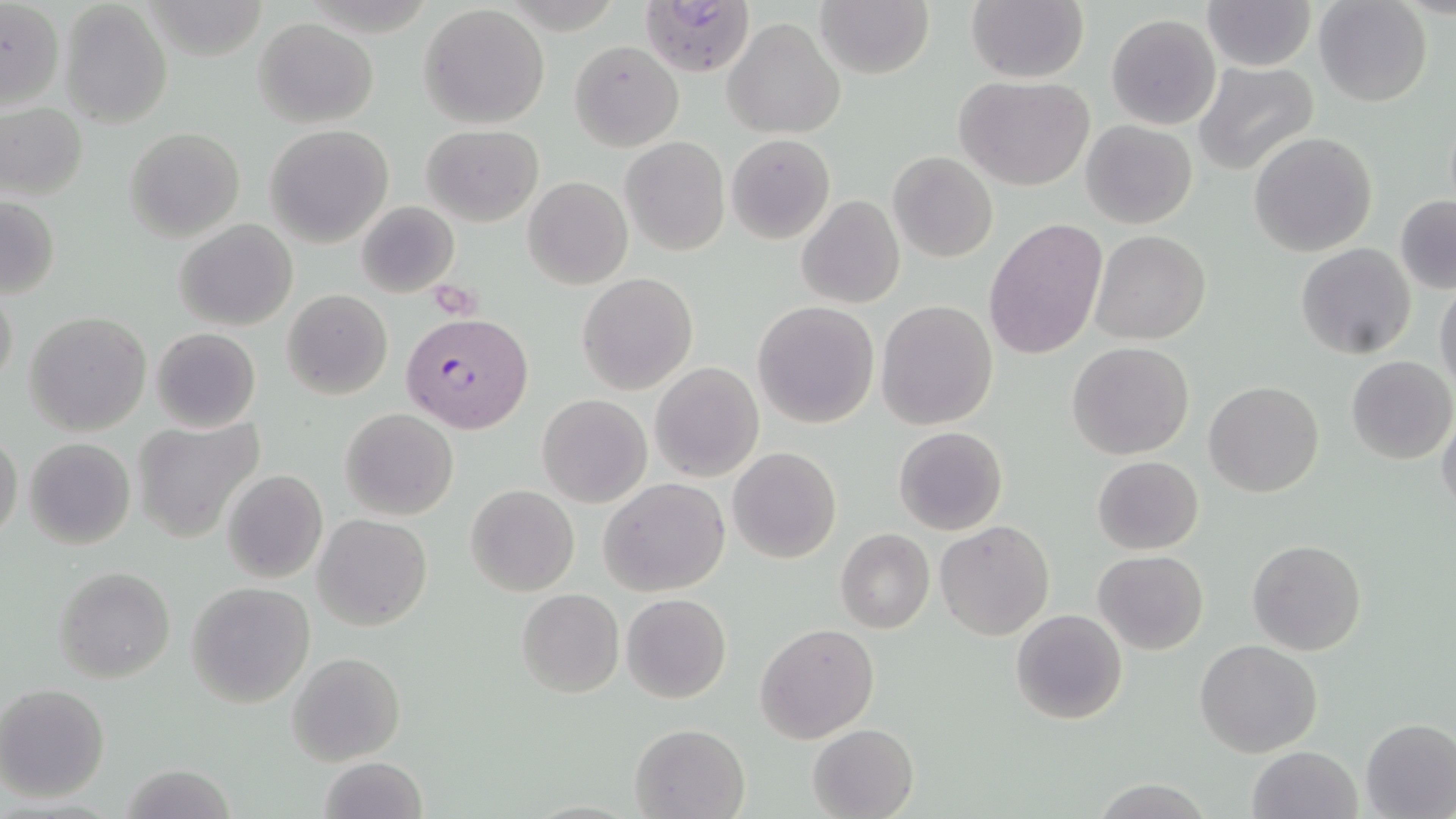
Summary:
  - Coordinate format: approximate bounding boxes as (x1,y1)-(x2,y2) corner pairs in pixels
  - Uninfected red blood cell locations: (0,0)-(65,114), (815,0)-(934,79), (966,0)-(1090,84), (1200,0)-(1318,71), (1312,0)-(1433,107), (61,2)-(172,127), (420,5)-(551,130), (1105,13)-(1222,131), (254,17)-(378,127), (723,17)-(845,140), (569,41)-(684,151), (1192,61)-(1321,176), (956,75)-(1097,190), (0,104)-(87,201), (1081,121)-(1197,230), (265,124)-(395,247), (422,125)-(544,226), (125,127)-(244,244), (1248,131)-(1379,258), (726,134)-(835,243), (619,136)-(731,255), (888,151)-(997,262), (523,175)-(632,289), (796,194)-(905,309), (1395,195)-(1456,294), (1,196)-(61,300), (355,201)-(459,297), (174,218)-(297,332), (983,218)-(1108,360), (1091,230)-(1211,345), (1296,243)-(1418,360), (577,274)-(698,395), (1434,281)-(1456,399), (1,282)-(18,392), (281,289)-(393,400), (876,299)-(998,430), (753,300)-(879,429), (24,311)-(150,435), (151,328)-(260,432), (1068,342)-(1195,460), (1346,356)-(1455,465), (649,361)-(764,483), (1204,380)-(1325,497), (537,394)-(652,508), (1436,407)-(1456,520), (339,408)-(460,521), (134,418)-(262,542), (894,426)-(1007,534), (0,432)-(24,539), (24,437)-(137,548), (728,447)-(843,564), (1091,455)-(1205,555), (223,469)-(329,584), (599,478)-(730,598), (465,485)-(580,597), (313,514)-(433,630), (935,521)-(1053,640), (835,529)-(934,634), (1247,538)-(1366,657), (1093,550)-(1208,654), (55,565)-(177,683), (185,583)-(316,708), (516,588)-(623,698), (621,593)-(732,704), (1011,609)-(1128,725), (756,623)-(879,743), (1195,639)-(1323,757), (287,651)-(407,767), (0,683)-(112,803), (1361,718)-(1456,818), (807,722)-(919,818), (629,723)-(750,818), (1247,746)-(1361,819), (317,756)-(430,818), (1092,779)-(1213,818)
  - Plasmodium falciparum-infected red blood cell locations: (639,0)-(760,78), (402,311)-(533,433)
  - Slide-level diagnosis: Plasmodium falciparum
  - Preparation: thin blood smear
  - Field of view: one of a larger specimen
  - Stain: May-Grünwald-Giemsa
  - Modality: optical microscopy
  - Magnification: 1000x
  - Image size: 1456×819 pixels